Locate and identify every blood parasite.
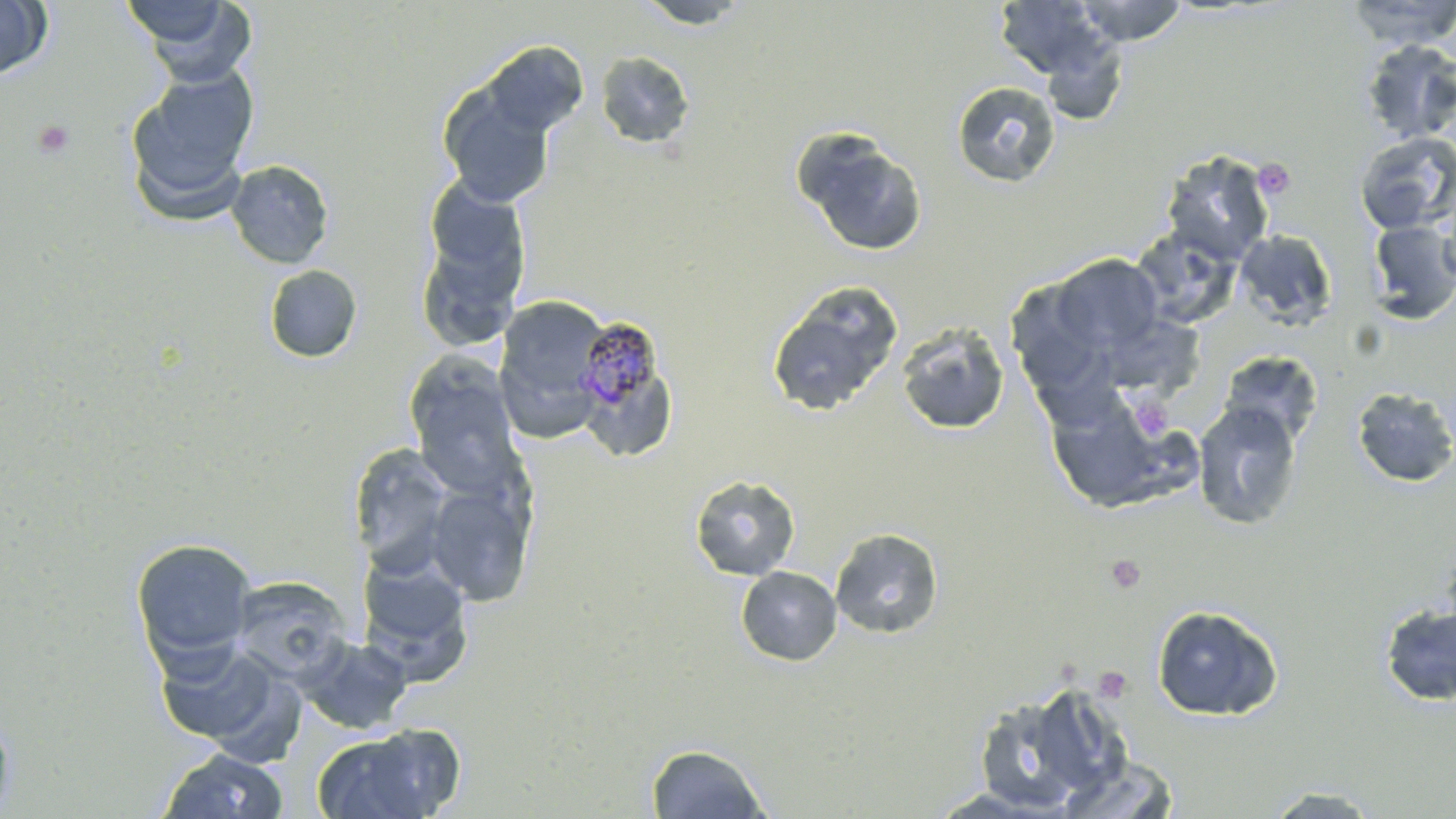
Approximate bounding boxes as [x1, y1, x2, y2] in pixels.
Plasmodium malariae-infected red blood cells: [572, 314, 660, 415].
No Plasmodium falciparum, Plasmodium ovale, Plasmodium vivax, Babesia divergens, or Trypanosoma brucei observed.

Summary:
  - Platelet locations: [33, 119, 75, 158], [1252, 158, 1295, 200], [1130, 397, 1172, 440], [1105, 554, 1146, 593], [1093, 667, 1132, 702]
  - Uninfected red blood cell locations: [0, 0, 53, 80], [128, 0, 258, 87], [633, 0, 754, 29], [1073, 0, 1188, 46], [1344, 0, 1456, 47], [993, 1, 1111, 79], [1042, 32, 1128, 126], [1359, 38, 1456, 143], [481, 41, 588, 137], [596, 50, 695, 150], [125, 66, 260, 216], [952, 81, 1060, 188], [438, 82, 556, 207], [793, 128, 927, 256], [1354, 131, 1456, 235], [1161, 150, 1275, 265], [226, 160, 334, 269], [422, 175, 531, 299], [1437, 183, 1456, 290], [1367, 221, 1456, 324], [1130, 228, 1242, 330], [415, 229, 526, 355], [1234, 230, 1337, 330], [1051, 254, 1163, 354], [264, 264, 363, 363], [767, 281, 903, 418], [1011, 281, 1095, 388], [493, 296, 614, 441], [895, 321, 1010, 435], [1027, 332, 1119, 440], [1218, 350, 1323, 447], [405, 353, 523, 495], [584, 376, 678, 460], [1351, 385, 1456, 488], [1042, 390, 1189, 512], [1192, 402, 1302, 530], [348, 443, 458, 576], [689, 474, 801, 581], [425, 482, 535, 606], [830, 527, 944, 639], [130, 537, 257, 669], [354, 552, 475, 683], [735, 566, 842, 666], [229, 575, 353, 684], [1378, 601, 1456, 707], [1151, 604, 1284, 722], [295, 635, 413, 736], [153, 639, 290, 751], [971, 684, 1123, 814], [0, 706, 16, 818], [312, 726, 460, 819], [646, 743, 771, 818], [156, 749, 289, 818], [1054, 756, 1184, 818], [1258, 787, 1388, 817]
  - Slide-level diagnosis: Plasmodium malariae
  - Magnification: 1000x
  - Preparation: thin blood film
  - Field of view: one of a larger specimen
  - Modality: light microscopy
  - Image size: 1456×819 pixels
  - Stain: May-Grünwald-Giemsa